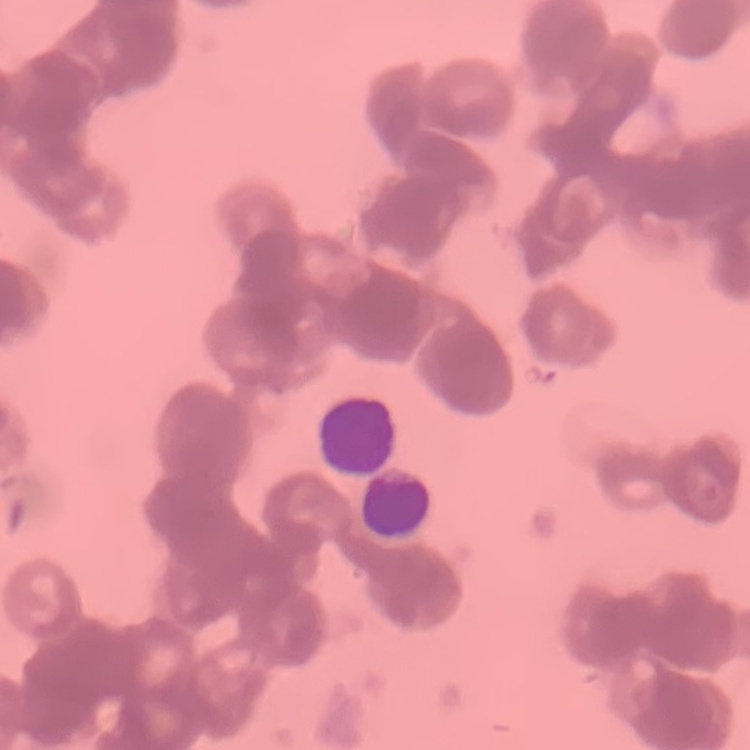

Summary:
  - Erythrocyte morphology: rouleaux formation
  - Stain: Field's or Giemsa
  - Image type: square crop of a larger photomicrograph
  - Preparation: thin blood smear